Assess this cell for malaria.
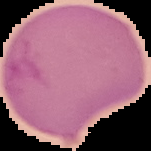

Parasitized.

Segmented cell region on a black background. From a thin blood smear. Image is 151×151 pixels.